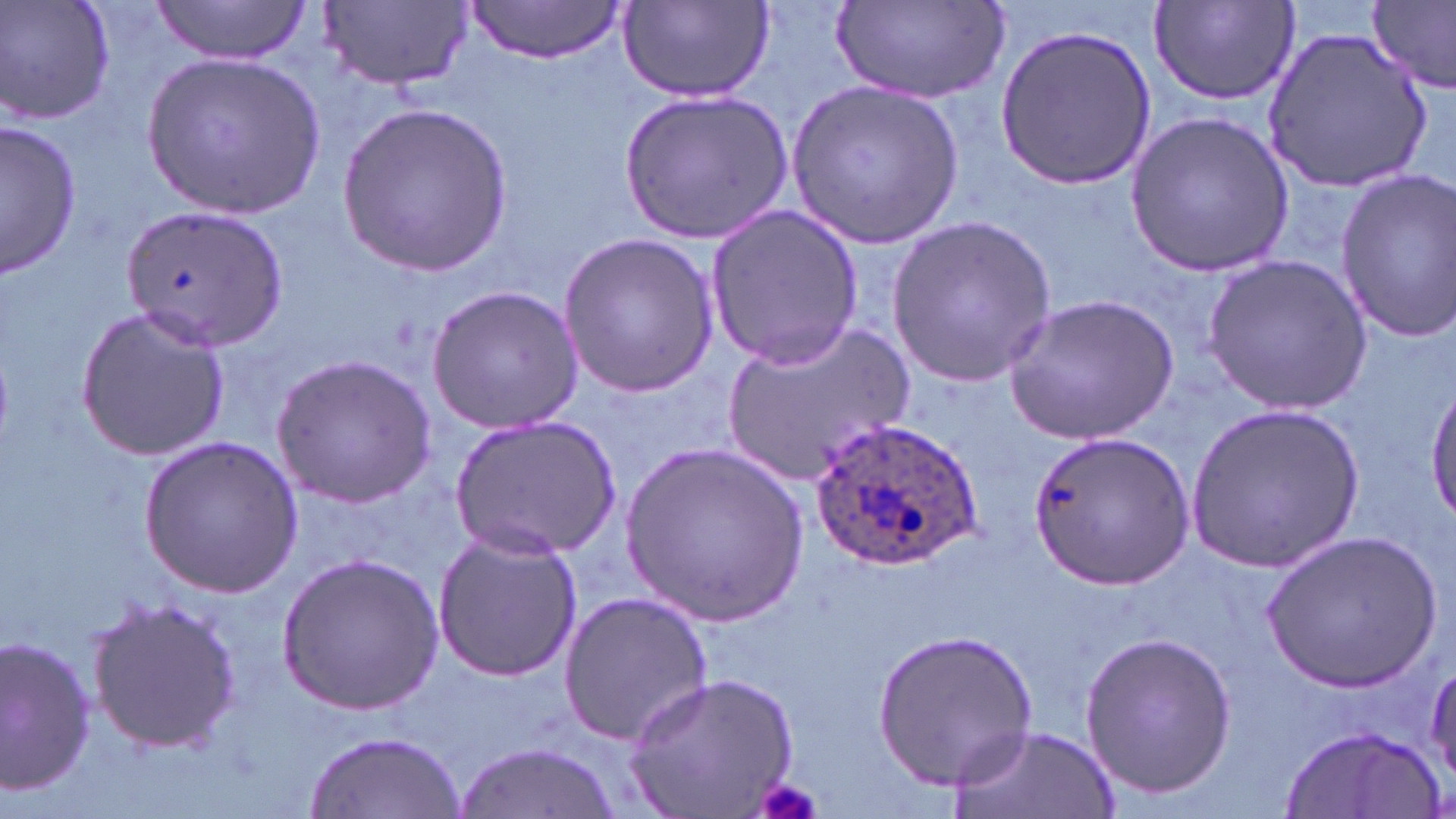
Summary:
  - Coordinate format: approximate bounding boxes as [x1, y1, x2, y2] in pixels
  - Plasmodium ovale-infected red blood cell locations: [808, 415, 983, 575]
  - Uninfected red blood cell locations: [2, 0, 116, 128], [149, 0, 313, 63], [316, 0, 471, 95], [460, 0, 632, 64], [619, 0, 773, 102], [833, 0, 1013, 105], [1370, 0, 1456, 94], [1148, 2, 1302, 106], [996, 25, 1157, 190], [1263, 26, 1435, 193], [144, 55, 325, 218], [789, 78, 963, 250], [620, 91, 791, 241], [338, 104, 513, 276], [1126, 110, 1294, 275], [1, 121, 82, 278], [1331, 170, 1456, 340], [119, 197, 291, 351], [704, 204, 864, 369], [886, 216, 1056, 387], [556, 232, 719, 398], [1204, 253, 1372, 413], [426, 284, 584, 435], [1004, 293, 1180, 446], [76, 304, 229, 461], [719, 318, 916, 487], [271, 354, 435, 508], [1427, 379, 1456, 520], [1184, 400, 1363, 576], [449, 416, 620, 559], [1025, 430, 1191, 591], [139, 434, 304, 597], [622, 445, 808, 627], [429, 523, 588, 685], [1264, 529, 1442, 694], [277, 552, 443, 715], [555, 588, 713, 746], [82, 594, 243, 757], [873, 626, 1042, 791], [1078, 628, 1237, 799], [0, 634, 97, 797], [624, 673, 800, 817], [946, 723, 1117, 819], [1279, 724, 1444, 817], [303, 729, 466, 818], [456, 741, 624, 819]
  - Platelet locations: [753, 776, 823, 819]
  - Slide-level diagnosis: Plasmodium ovale
  - Field of view: single
  - Magnification: 1000x
  - Image size: 1456×819 pixels
  - Modality: optical microscopy
  - Stain: May-Grünwald-Giemsa
  - Preparation: thin blood film